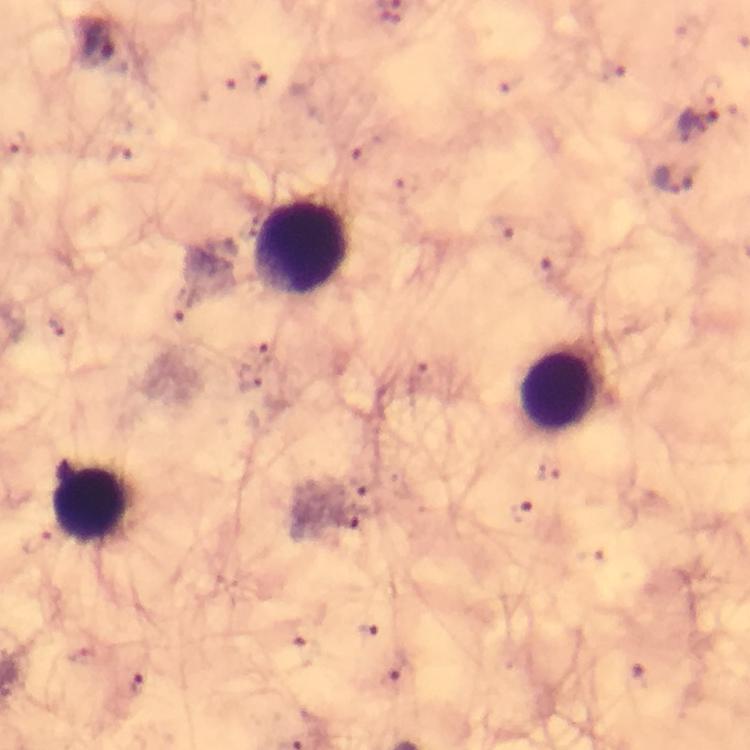

immersion_oil: applied
capture: smartphone camera through the microscope
stain: Giemsa
malaria_parasite_locations: 'approximate centers as (x, y) in pixels: (96, 39), (699, 123), (122, 154), (674, 178), (521, 510), (349, 517), (139, 686)'
leukocyte_locations: 'approximate centers as (x, y) in pixels: (303, 248), (561, 390), (94, 505)'
image_size: 750×750 pixels
cropped_from: one field of view
context: from a malaria diagnostic workup
preparation: thick blood film
magnification: 100x